State the blood parasite species.
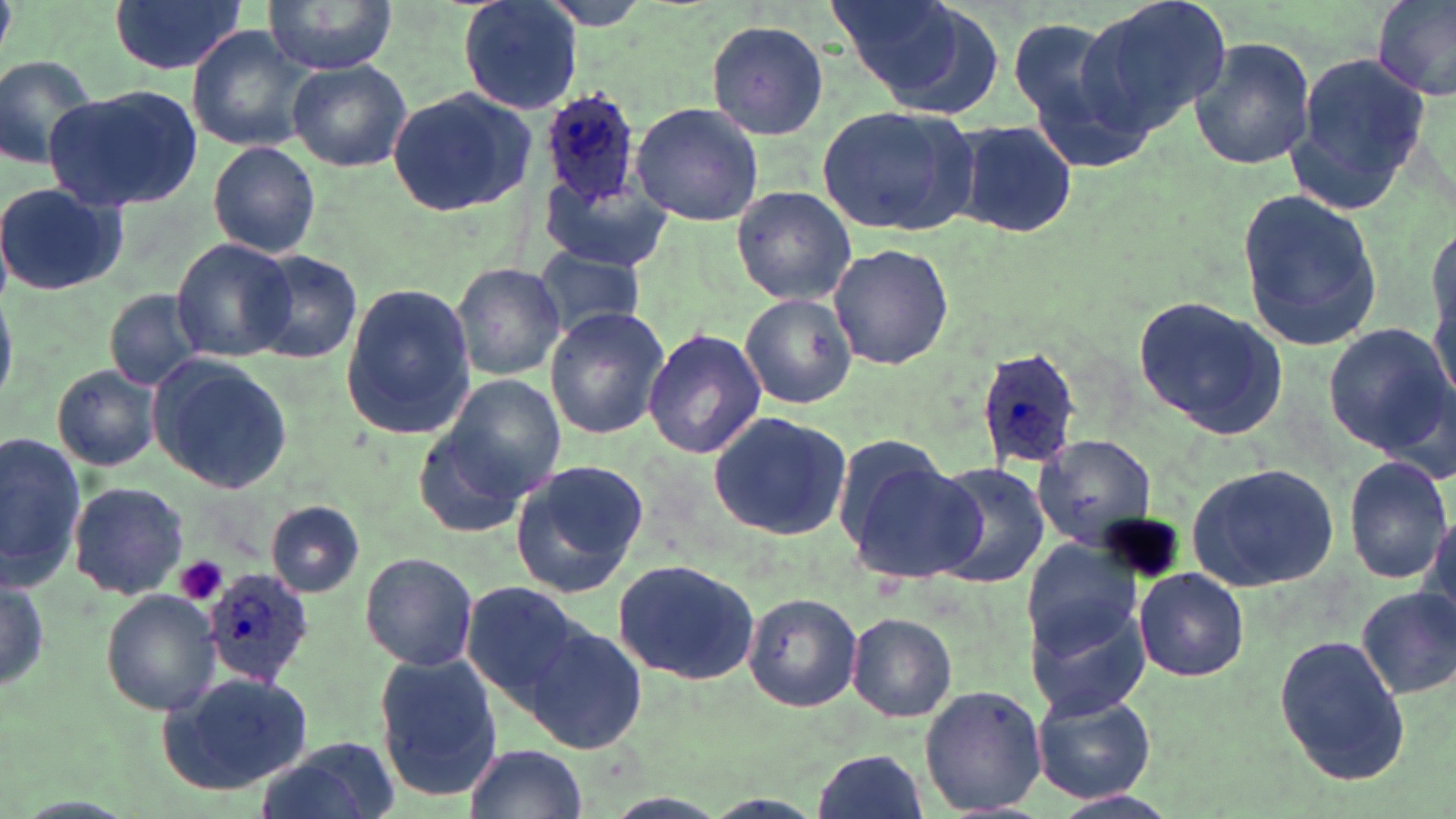

Plasmodium ovale.

Summary:
  - Coordinate format: approximate bounding boxes as (x1, y1, x2, y2) in pixels
  - Platelet locations: (175, 555, 228, 607)
  - Plasmodium ovale-infected red blood cell locations: (538, 89, 646, 206), (975, 346, 1082, 470), (204, 567, 317, 684)
  - Uninfected red blood cell locations: (108, 0, 246, 77), (262, 0, 398, 73), (458, 0, 583, 115), (825, 0, 990, 110), (1077, 0, 1230, 139), (1372, 0, 1456, 102), (126, 5, 295, 115), (1007, 14, 1146, 164), (704, 21, 831, 139), (187, 26, 316, 151), (1189, 34, 1317, 173), (1283, 49, 1430, 217), (0, 52, 101, 171), (288, 62, 412, 172), (44, 84, 202, 211), (387, 86, 534, 215), (631, 102, 766, 225), (816, 104, 981, 237), (955, 118, 1076, 239), (208, 141, 319, 258), (540, 178, 668, 271), (0, 181, 130, 298), (730, 184, 856, 307), (1237, 185, 1387, 353), (1425, 215, 1456, 405), (170, 239, 297, 360), (828, 242, 954, 370), (247, 249, 363, 364), (533, 249, 646, 339), (451, 260, 567, 381), (339, 284, 476, 441), (105, 288, 207, 390), (738, 291, 856, 409), (1132, 296, 1289, 442), (545, 308, 668, 438), (1323, 322, 1453, 456), (643, 327, 767, 459), (149, 356, 293, 495), (50, 365, 162, 473), (435, 372, 566, 500), (707, 411, 852, 541), (412, 425, 535, 539), (0, 431, 85, 589), (1031, 434, 1159, 550), (1345, 454, 1451, 585), (507, 460, 650, 599), (848, 460, 988, 584), (929, 462, 1051, 588), (1185, 462, 1341, 592), (69, 481, 188, 600), (266, 501, 364, 597), (1420, 507, 1455, 632), (1019, 545, 1144, 708), (359, 551, 479, 672), (611, 556, 760, 684), (1133, 568, 1248, 682), (0, 573, 50, 695), (459, 581, 591, 710), (1355, 586, 1456, 699), (101, 591, 222, 716), (743, 591, 862, 712), (846, 612, 956, 722), (526, 624, 649, 754), (1273, 630, 1410, 785), (376, 654, 505, 801), (161, 670, 314, 795), (918, 683, 1046, 815), (1031, 690, 1157, 803), (256, 739, 397, 819), (465, 743, 587, 819), (811, 749, 927, 819)
  - Field of view: single
  - Stain: May-Grünwald-Giemsa
  - Preparation: thin blood film
  - Image size: 1456×819 pixels
  - Magnification: 1000x
  - Modality: light microscopy